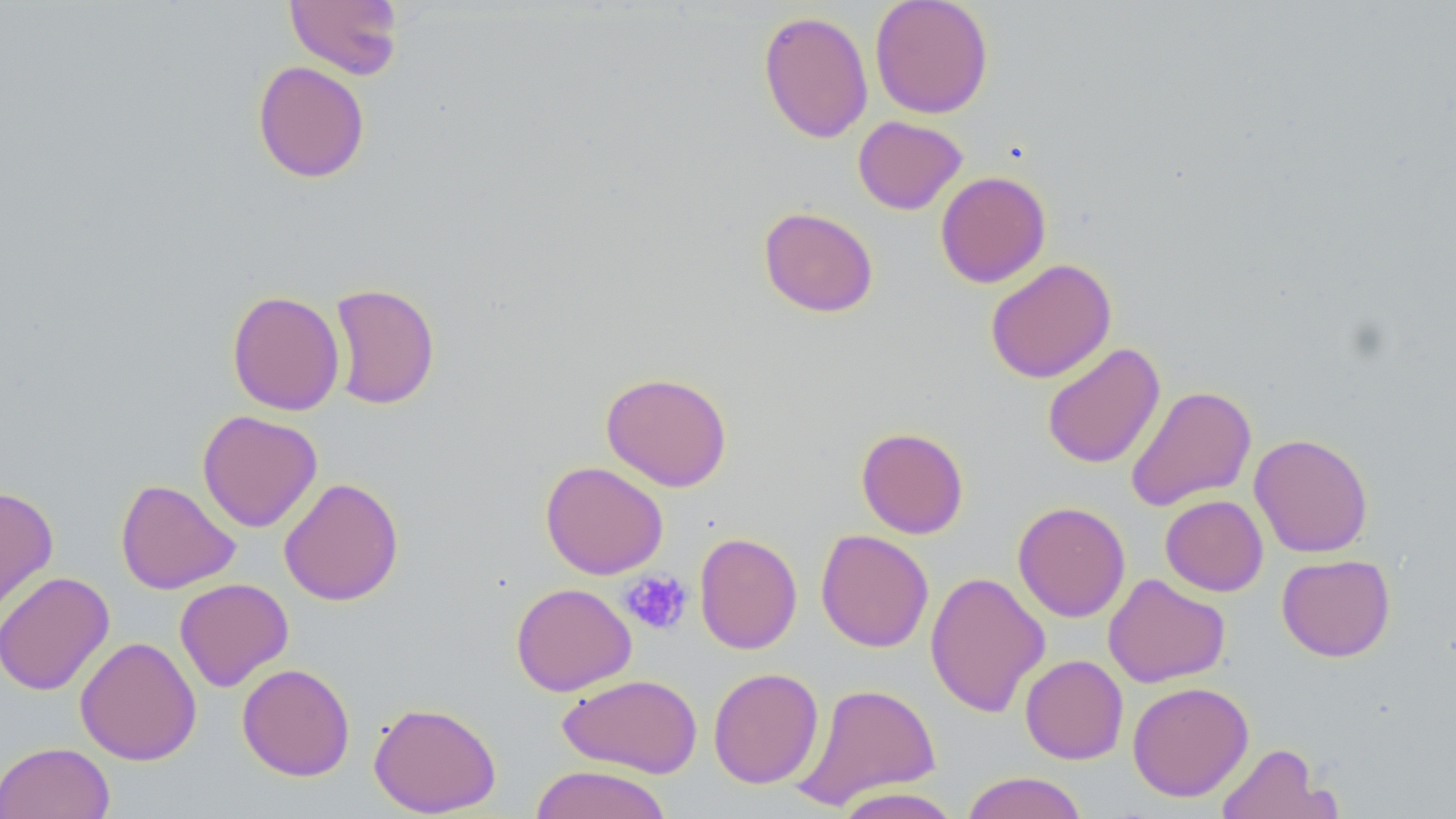
Summary:
  - Coordinate format: approximate bounding boxes as named x1/y1/x2/y2 corners in pixels
  - Uninfected red blood cell locations: (x1=284, y1=0, x2=404, y2=80), (x1=870, y1=0, x2=994, y2=118), (x1=758, y1=10, x2=873, y2=144), (x1=252, y1=60, x2=370, y2=183), (x1=853, y1=116, x2=967, y2=214), (x1=935, y1=170, x2=1051, y2=288), (x1=758, y1=206, x2=879, y2=317), (x1=985, y1=258, x2=1116, y2=383), (x1=328, y1=282, x2=440, y2=410), (x1=227, y1=290, x2=345, y2=416), (x1=1041, y1=342, x2=1165, y2=469), (x1=600, y1=371, x2=733, y2=491), (x1=1126, y1=384, x2=1256, y2=511), (x1=197, y1=410, x2=323, y2=532), (x1=856, y1=426, x2=969, y2=539), (x1=1249, y1=433, x2=1374, y2=558), (x1=540, y1=460, x2=668, y2=579), (x1=279, y1=477, x2=403, y2=606), (x1=115, y1=479, x2=240, y2=594), (x1=0, y1=485, x2=58, y2=621), (x1=1160, y1=494, x2=1268, y2=596), (x1=1012, y1=501, x2=1130, y2=622), (x1=815, y1=529, x2=934, y2=652), (x1=694, y1=532, x2=802, y2=654), (x1=1277, y1=553, x2=1395, y2=662), (x1=0, y1=570, x2=115, y2=696), (x1=925, y1=571, x2=1050, y2=718), (x1=1103, y1=573, x2=1230, y2=688), (x1=174, y1=578, x2=293, y2=691), (x1=510, y1=582, x2=636, y2=696), (x1=75, y1=636, x2=201, y2=765), (x1=1020, y1=654, x2=1128, y2=764), (x1=237, y1=663, x2=355, y2=781), (x1=708, y1=667, x2=824, y2=789), (x1=558, y1=673, x2=703, y2=778), (x1=1127, y1=681, x2=1254, y2=801), (x1=792, y1=682, x2=941, y2=810), (x1=368, y1=701, x2=502, y2=817), (x1=0, y1=741, x2=115, y2=819), (x1=1214, y1=742, x2=1340, y2=819), (x1=529, y1=764, x2=672, y2=819), (x1=960, y1=771, x2=1089, y2=819), (x1=832, y1=786, x2=963, y2=819)
  - Platelet locations: (x1=621, y1=570, x2=692, y2=635)
  - Slide-level diagnosis: no evidence of blood parasites
  - Image size: 1456×819 pixels
  - Magnification: 1000x
  - Field of view: one of a larger specimen
  - Stain: May-Grünwald-Giemsa
  - Modality: optical microscopy
  - Preparation: thin blood film